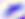
Captured at 400x magnification. Micrograph. Toxoplasma gondii is seen.